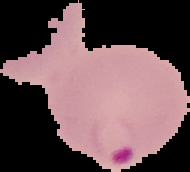 From a thin blood smear. Malaria status: parasitized. Image is 190×172 pixels. The area outside the segmented cell region is set to black.